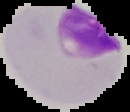

{
  "image_size": "130×112 pixels",
  "preparation": "thin blood film",
  "image_type": "cell region segmented out of the field of view; surrounding area masked to black",
  "result": "malaria parasites identified"
}